Report the malaria status of this cell.
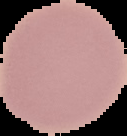

Uninfected.

Summary:
  - Image type: segmented cell region on a black background
  - Image size: 127×136 pixels
  - Preparation: thin blood smear